Assess this cell for malaria.
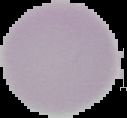
Uninfected.

Summary:
  - Image type: cell region segmented out of the field of view; surrounding area masked to black
  - Preparation: thin blood film
  - Image size: 127×118 pixels